Assess for malaria.
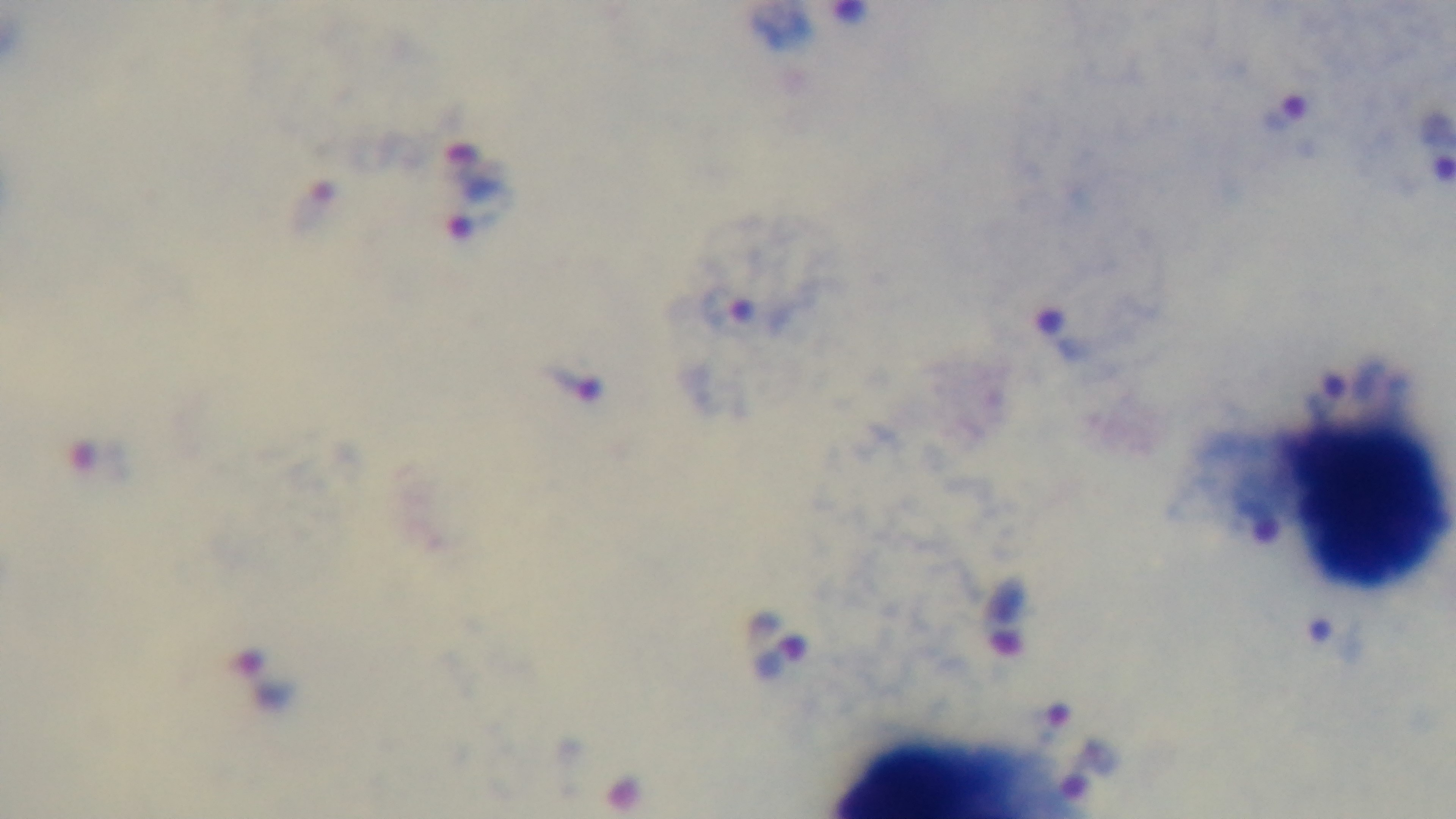
It is infected.

field of view = single
modality = light microscopy
capture = mounted 4K digital camera
objective = 100x oil immersion
stain = Giemsa
preparation = thick blood film